Classify this cell by malaria status.
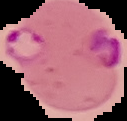

It is parasitized.

{
  "image_type": "segmented cell region on a black background",
  "preparation": "thin blood smear",
  "image_size": "127×121 pixels"
}